Outline each Plasmodium vivax-infected red blood cell.
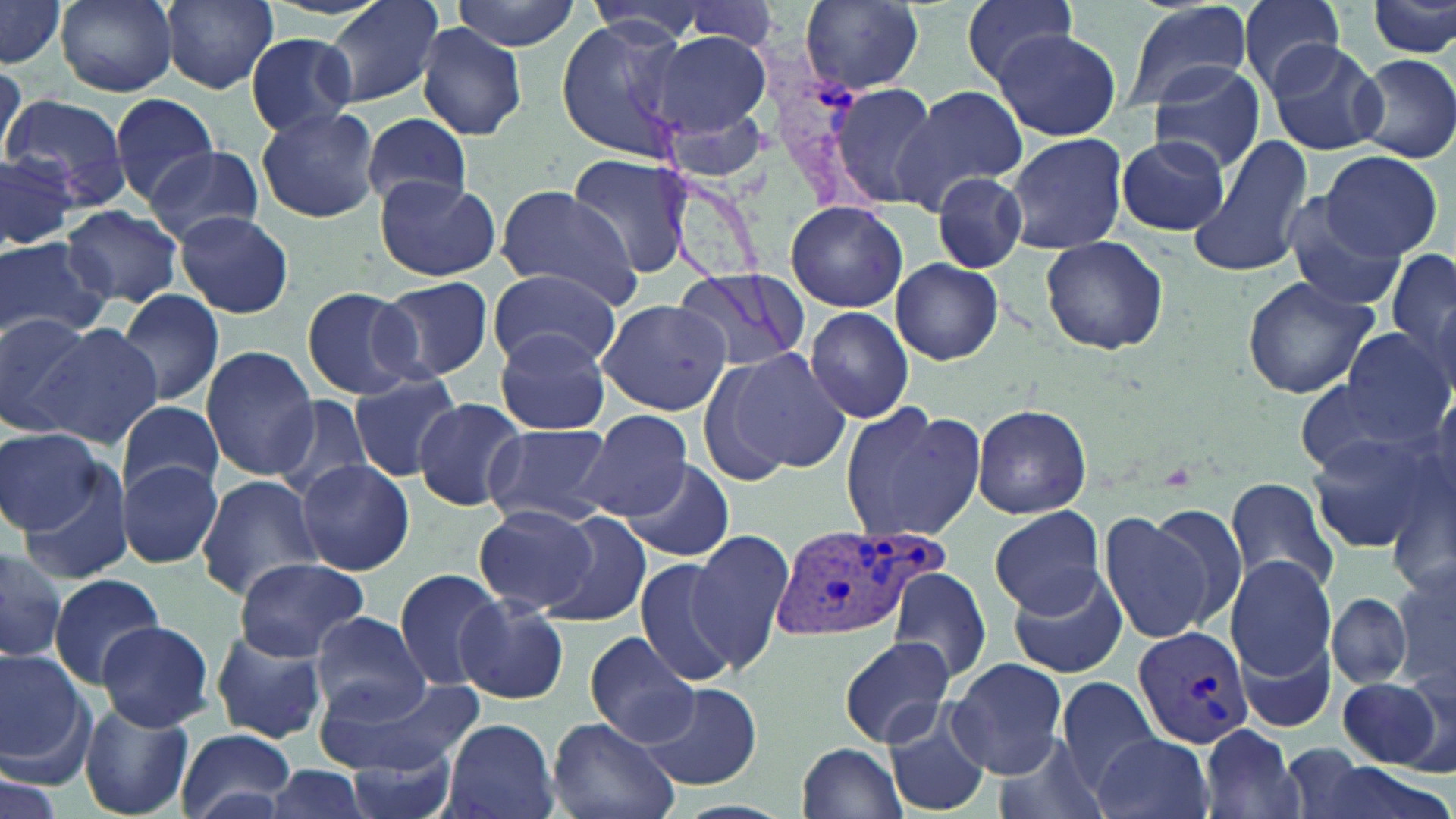

Approximate bounding boxes as (x1,y1)-(x2,y2) corner pairs in pixels.
Plasmodium vivax-infected red blood cells: (773,525)-(953,644), (1131,625)-(1254,751).

Summary:
  - Uninfected red blood cell locations: (56,0)-(177,95), (159,0)-(284,96), (322,0)-(448,110), (451,0)-(582,50), (584,0)-(717,45), (801,0)-(925,92), (956,0)-(1082,89), (1122,0)-(1255,115), (1233,0)-(1348,94), (1369,0)-(1455,61), (0,1)-(64,68), (677,2)-(783,54), (555,19)-(692,163), (413,22)-(526,141), (993,29)-(1122,141), (648,30)-(773,146), (247,31)-(359,136), (1264,38)-(1387,157), (1352,53)-(1456,163), (1148,61)-(1268,175), (0,63)-(28,174), (832,83)-(942,208), (894,85)-(1027,208), (5,91)-(129,207), (111,92)-(220,204), (256,104)-(382,225), (360,113)-(474,211), (1001,131)-(1128,253), (1116,134)-(1229,236), (1187,134)-(1315,282), (144,146)-(265,245), (0,149)-(81,253), (1319,150)-(1445,261), (566,153)-(694,280), (931,171)-(1027,272), (372,177)-(503,281), (495,185)-(642,303), (1276,194)-(1410,313), (784,201)-(911,311), (63,206)-(184,306), (173,210)-(294,319), (1041,235)-(1169,355), (0,238)-(109,344), (1385,246)-(1456,372), (892,258)-(1005,365), (672,267)-(809,375), (486,270)-(622,369), (1240,274)-(1382,400), (376,276)-(495,381), (300,287)-(420,398), (115,288)-(225,407), (596,297)-(733,417), (805,305)-(915,424), (0,310)-(98,437), (29,322)-(161,449), (493,329)-(612,435), (1340,331)-(1452,447), (201,347)-(319,479), (716,348)-(851,478), (348,370)-(467,482), (1295,370)-(1434,482), (270,394)-(373,504), (412,399)-(533,512), (970,402)-(1092,518), (118,403)-(224,498), (839,403)-(986,543), (576,408)-(694,522), (485,422)-(612,528), (0,426)-(105,535), (1306,430)-(1443,553), (294,459)-(414,575), (622,459)-(736,563), (117,461)-(223,569), (15,467)-(136,585), (196,475)-(325,600), (1226,475)-(1342,596), (1142,499)-(1253,633), (473,506)-(600,614), (990,507)-(1108,614), (1098,508)-(1219,645), (533,510)-(654,627), (688,530)-(796,669), (0,542)-(67,663), (1226,555)-(1339,683), (632,556)-(740,686), (232,558)-(368,662), (1392,560)-(1456,699), (889,565)-(991,687), (1005,565)-(1128,679), (395,568)-(508,691), (46,574)-(170,690), (1328,592)-(1412,688), (455,597)-(569,705), (311,611)-(431,719), (96,621)-(215,732), (208,630)-(328,745), (586,632)-(700,748), (1240,633)-(1336,736), (839,637)-(955,748), (0,647)-(88,772), (947,658)-(1066,776), (324,674)-(482,772), (1337,677)-(1443,769), (1055,678)-(1165,794), (640,685)-(762,791), (79,700)-(194,817), (880,704)-(992,816), (442,717)-(558,819), (547,718)-(680,819), (1197,726)-(1306,819), (177,729)-(297,818), (989,732)-(1108,819), (1094,732)-(1212,819), (343,739)-(458,819), (796,740)-(909,818), (1278,742)-(1376,819), (261,763)-(371,819), (0,769)-(64,819)
  - Slide-level diagnosis: Plasmodium vivax
  - Stain: May-Grünwald-Giemsa
  - Modality: optical microscopy
  - Image size: 1456×819 pixels
  - Field of view: one of a larger specimen
  - Preparation: thin blood smear
  - Magnification: 1000x